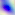

Micrograph. Toxoplasma gondii is seen. 400x magnification.